Report the malaria status of this cell.
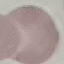

Uninfected.

stain: Giemsa
preparation: thin blood film
image_type: cell patch, automatically extracted from a larger field of view and resized to 64 × 64 pixels
capture: smartphone through the microscope eyepiece